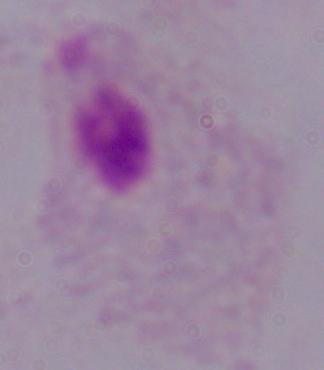
Summary:
  - Magnification: 1000x
  - Modality: photomicrograph
  - Identification: trichomonad